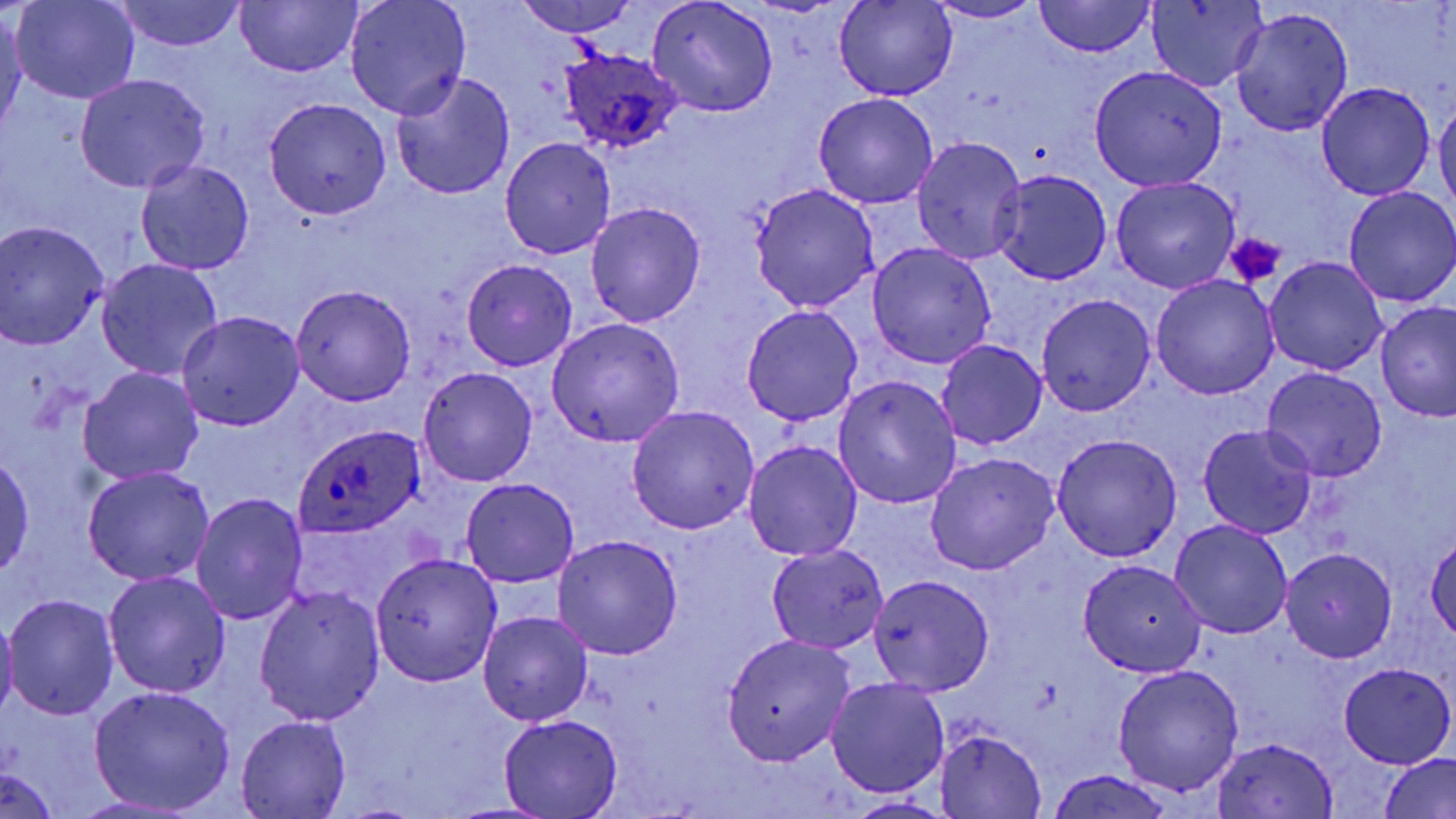 Approximate bounding boxes as named x1/y1/x2/y2 corners in pixels. Platelet locations: (x1=1226, y1=233, x2=1285, y2=289). Plasmodium ovale-infected red blood cell locations: (x1=558, y1=47, x2=683, y2=154), (x1=294, y1=426, x2=422, y2=539). Uninfected red blood cell locations: (x1=10, y1=0, x2=139, y2=103), (x1=517, y1=0, x2=640, y2=35), (x1=647, y1=0, x2=780, y2=117), (x1=1037, y1=0, x2=1154, y2=58), (x1=118, y1=1, x2=245, y2=51), (x1=237, y1=1, x2=362, y2=77), (x1=343, y1=1, x2=472, y2=119), (x1=925, y1=1, x2=1047, y2=23), (x1=1146, y1=1, x2=1266, y2=91), (x1=834, y1=3, x2=958, y2=102), (x1=0, y1=7, x2=26, y2=140), (x1=1231, y1=7, x2=1352, y2=137), (x1=1089, y1=66, x2=1226, y2=190), (x1=389, y1=69, x2=516, y2=201), (x1=75, y1=72, x2=210, y2=192), (x1=1317, y1=83, x2=1434, y2=200), (x1=813, y1=92, x2=938, y2=209), (x1=264, y1=97, x2=391, y2=218), (x1=1433, y1=97, x2=1456, y2=217), (x1=913, y1=136, x2=1027, y2=263), (x1=500, y1=137, x2=616, y2=259), (x1=135, y1=160, x2=255, y2=275), (x1=991, y1=170, x2=1113, y2=283), (x1=1109, y1=177, x2=1240, y2=294), (x1=749, y1=183, x2=880, y2=313), (x1=1344, y1=187, x2=1456, y2=307), (x1=586, y1=202, x2=707, y2=327), (x1=0, y1=222, x2=110, y2=349), (x1=867, y1=242, x2=996, y2=370), (x1=1264, y1=256, x2=1389, y2=376), (x1=97, y1=259, x2=225, y2=380), (x1=461, y1=259, x2=579, y2=371), (x1=1150, y1=274, x2=1279, y2=398), (x1=290, y1=283, x2=418, y2=406), (x1=1035, y1=294, x2=1156, y2=416), (x1=1374, y1=302, x2=1456, y2=421), (x1=741, y1=304, x2=863, y2=427), (x1=176, y1=311, x2=305, y2=431), (x1=547, y1=318, x2=685, y2=447), (x1=936, y1=340, x2=1047, y2=452), (x1=79, y1=366, x2=203, y2=485), (x1=1261, y1=366, x2=1388, y2=481), (x1=418, y1=367, x2=538, y2=487), (x1=833, y1=375, x2=962, y2=509), (x1=627, y1=405, x2=758, y2=535), (x1=1197, y1=424, x2=1318, y2=538), (x1=1051, y1=432, x2=1183, y2=561), (x1=743, y1=440, x2=862, y2=561), (x1=924, y1=452, x2=1060, y2=575), (x1=1, y1=453, x2=35, y2=581), (x1=83, y1=466, x2=215, y2=586), (x1=461, y1=478, x2=580, y2=588), (x1=191, y1=491, x2=309, y2=625), (x1=1169, y1=519, x2=1293, y2=640), (x1=1427, y1=534, x2=1456, y2=642), (x1=554, y1=535, x2=682, y2=660), (x1=767, y1=544, x2=889, y2=653), (x1=1281, y1=547, x2=1397, y2=662), (x1=370, y1=551, x2=501, y2=686), (x1=1077, y1=559, x2=1207, y2=677), (x1=103, y1=570, x2=231, y2=699), (x1=868, y1=575, x2=996, y2=697), (x1=253, y1=585, x2=387, y2=727), (x1=4, y1=594, x2=119, y2=721), (x1=479, y1=610, x2=593, y2=727), (x1=0, y1=614, x2=19, y2=723), (x1=722, y1=633, x2=855, y2=766), (x1=1338, y1=662, x2=1455, y2=767), (x1=1111, y1=666, x2=1243, y2=796), (x1=825, y1=677, x2=950, y2=798), (x1=87, y1=685, x2=237, y2=814), (x1=499, y1=714, x2=625, y2=818), (x1=234, y1=716, x2=351, y2=819), (x1=935, y1=730, x2=1046, y2=817), (x1=1210, y1=737, x2=1340, y2=817), (x1=1380, y1=753, x2=1456, y2=819), (x1=0, y1=765, x2=62, y2=817), (x1=1046, y1=768, x2=1174, y2=819), (x1=843, y1=796, x2=955, y2=818). Slide-level diagnosis: Plasmodium ovale. Single field of view. Image is 1456×819 pixels. Thin blood smear. Captured at 1000x magnification. Light microscopy. May-Grünwald-Giemsa-stained preparation.